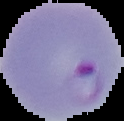
From a thin blood smear. Image is 124×121 pixels. Malaria status: parasitized. Segmented cell region on a black background.